Locate every malaria parasite.
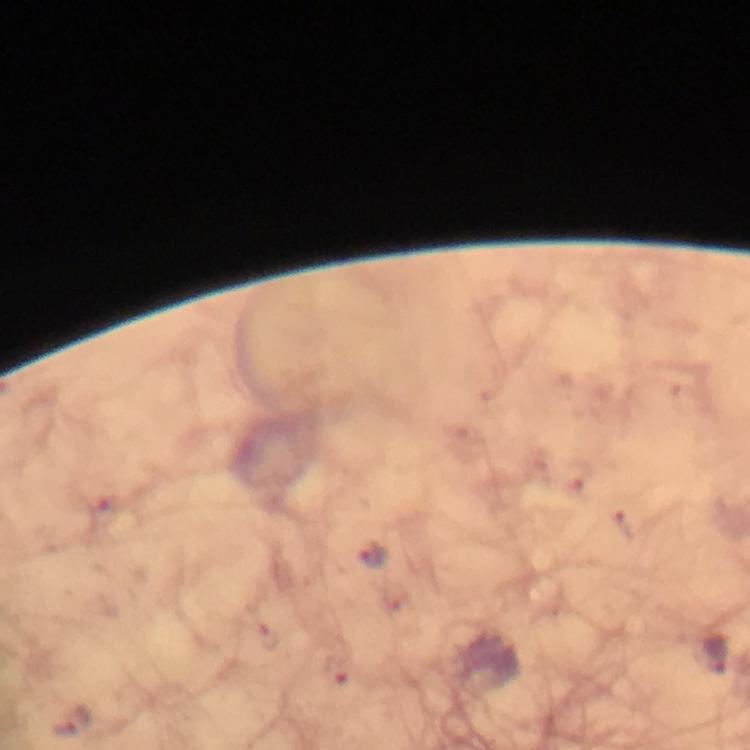
Approximate object centers, in pixels from the top-left corner.
Malaria parasites: (x=577, y=475), (x=626, y=524), (x=372, y=555), (x=717, y=653), (x=337, y=672), (x=65, y=728).

Summary:
  - Stain: Giemsa
  - Immersion oil: used
  - Capture: smartphone mounted on the microscope
  - Preparation: thick blood film
  - Context: from a malaria diagnostic workup
  - Magnification: 100x
  - Image size: 750×750 pixels
  - Cropped from: a single field of view